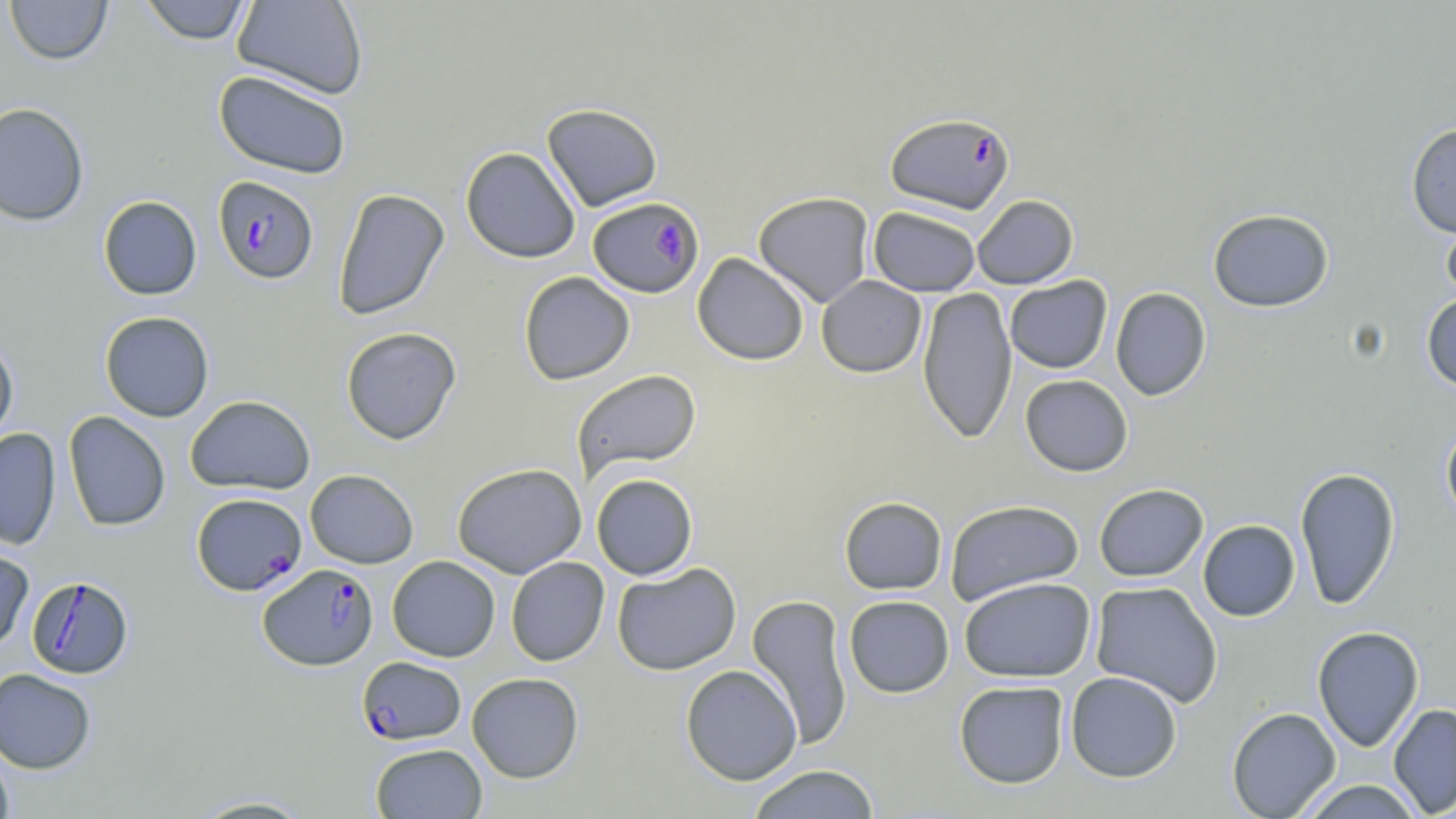

Approximate bounding boxes as named x1/y1/x2/y2 corners in pixels. Uninfected red blood cell locations: (x1=4, y1=0, x2=113, y2=65), (x1=138, y1=0, x2=254, y2=45), (x1=233, y1=0, x2=368, y2=99), (x1=213, y1=69, x2=352, y2=179), (x1=0, y1=102, x2=90, y2=226), (x1=542, y1=103, x2=663, y2=212), (x1=1405, y1=122, x2=1456, y2=238), (x1=460, y1=146, x2=580, y2=263), (x1=332, y1=188, x2=450, y2=321), (x1=753, y1=191, x2=875, y2=307), (x1=97, y1=195, x2=202, y2=300), (x1=971, y1=195, x2=1078, y2=289), (x1=1440, y1=204, x2=1456, y2=306), (x1=868, y1=206, x2=982, y2=296), (x1=1207, y1=208, x2=1335, y2=312), (x1=692, y1=252, x2=809, y2=366), (x1=519, y1=271, x2=635, y2=385), (x1=816, y1=275, x2=926, y2=378), (x1=1005, y1=275, x2=1112, y2=374), (x1=917, y1=286, x2=1017, y2=445), (x1=1110, y1=286, x2=1211, y2=401), (x1=1421, y1=292, x2=1456, y2=393), (x1=100, y1=311, x2=214, y2=421), (x1=341, y1=326, x2=462, y2=445), (x1=0, y1=335, x2=19, y2=451), (x1=571, y1=369, x2=702, y2=481), (x1=1020, y1=374, x2=1133, y2=476), (x1=185, y1=395, x2=316, y2=495), (x1=63, y1=411, x2=171, y2=532), (x1=1440, y1=420, x2=1456, y2=529), (x1=0, y1=428, x2=61, y2=551), (x1=452, y1=462, x2=587, y2=578), (x1=1294, y1=467, x2=1401, y2=610), (x1=305, y1=469, x2=419, y2=568), (x1=591, y1=474, x2=698, y2=580), (x1=1094, y1=483, x2=1208, y2=582), (x1=839, y1=496, x2=948, y2=596), (x1=944, y1=499, x2=1085, y2=605), (x1=1198, y1=519, x2=1301, y2=621), (x1=0, y1=543, x2=34, y2=653), (x1=387, y1=555, x2=500, y2=662), (x1=506, y1=557, x2=609, y2=666), (x1=612, y1=563, x2=741, y2=676), (x1=958, y1=576, x2=1097, y2=683), (x1=1090, y1=581, x2=1223, y2=708), (x1=746, y1=594, x2=854, y2=749), (x1=844, y1=595, x2=954, y2=698), (x1=1312, y1=626, x2=1424, y2=752), (x1=680, y1=665, x2=802, y2=785), (x1=0, y1=668, x2=97, y2=773), (x1=1065, y1=671, x2=1183, y2=782), (x1=467, y1=672, x2=584, y2=783), (x1=954, y1=681, x2=1070, y2=788), (x1=1388, y1=703, x2=1456, y2=817), (x1=1226, y1=707, x2=1341, y2=819), (x1=370, y1=743, x2=487, y2=818), (x1=0, y1=744, x2=15, y2=819), (x1=745, y1=764, x2=881, y2=819), (x1=1298, y1=780, x2=1425, y2=818), (x1=185, y1=795, x2=319, y2=818). Plasmodium falciparum-infected red blood cell locations: (x1=885, y1=112, x2=1015, y2=214), (x1=212, y1=176, x2=319, y2=285), (x1=588, y1=196, x2=704, y2=298), (x1=191, y1=492, x2=306, y2=595), (x1=257, y1=563, x2=379, y2=671), (x1=26, y1=575, x2=133, y2=679), (x1=357, y1=656, x2=466, y2=745). Slide-level diagnosis: Plasmodium falciparum. 1000x magnification. Light microscopy. Image is 1456×819 pixels. Thin blood film. One field of a larger specimen. May-Grünwald-Giemsa-stained preparation.